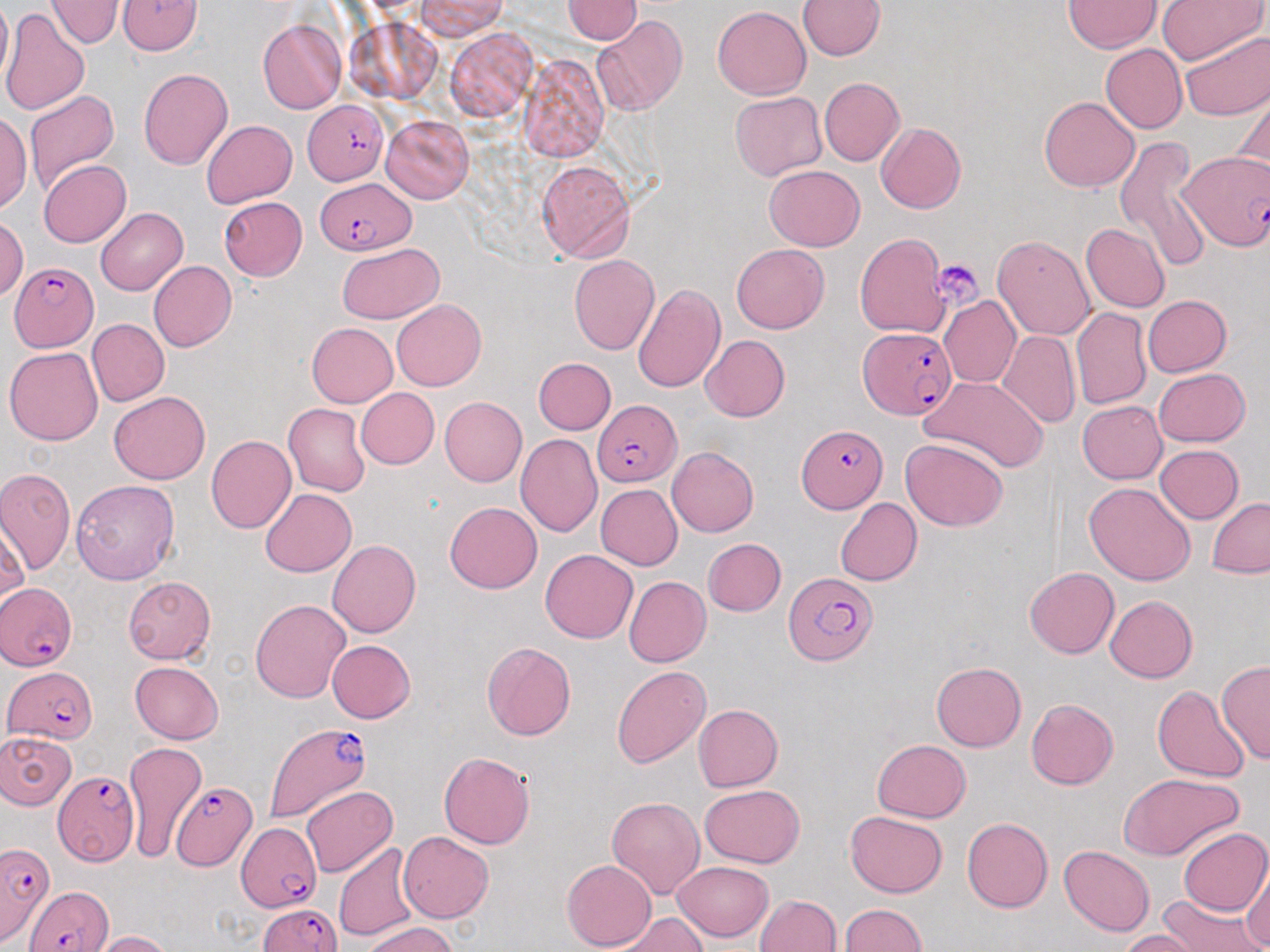
Summary:
  - Coordinate format: approximate bounding boxes as (x1, y1, x2, y2) in pixels
  - Uninfected red blood cell locations: (0, 0, 11, 91), (118, 0, 202, 55), (417, 0, 506, 39), (562, 0, 642, 45), (799, 0, 886, 60), (1155, 0, 1265, 67), (46, 1, 123, 49), (1063, 1, 1162, 53), (712, 5, 811, 98), (2, 9, 90, 115), (593, 15, 688, 118), (258, 17, 346, 114), (347, 18, 442, 104), (446, 27, 538, 122), (1180, 28, 1270, 120), (1100, 44, 1188, 133), (518, 54, 609, 161), (138, 68, 233, 170), (819, 78, 904, 166), (23, 89, 120, 198), (730, 91, 828, 182), (1234, 92, 1270, 186), (1039, 96, 1140, 192), (0, 114, 31, 211), (380, 115, 474, 203), (202, 119, 297, 208), (876, 123, 966, 213), (1114, 136, 1210, 271), (38, 160, 131, 247), (537, 161, 635, 262), (763, 166, 865, 252), (218, 196, 307, 281), (95, 207, 188, 295), (0, 216, 27, 301), (1081, 223, 1170, 313), (854, 232, 949, 339), (992, 235, 1095, 339), (337, 243, 444, 322), (731, 244, 829, 333), (569, 255, 660, 355), (149, 261, 236, 351), (632, 283, 726, 394), (939, 295, 1021, 387), (1143, 295, 1231, 378), (392, 299, 487, 391), (1071, 308, 1152, 410), (86, 319, 169, 406), (307, 323, 398, 406), (998, 330, 1080, 428), (700, 335, 791, 422), (4, 346, 103, 446), (533, 357, 616, 435), (1153, 368, 1250, 447), (918, 375, 1050, 473), (356, 388, 440, 469), (108, 393, 209, 484), (439, 397, 527, 486), (1077, 400, 1167, 483), (283, 402, 371, 497), (206, 434, 297, 533), (515, 434, 603, 536), (900, 438, 1009, 532), (1153, 444, 1245, 524), (667, 447, 759, 537), (0, 466, 75, 574), (70, 480, 179, 585), (1083, 482, 1196, 586), (595, 484, 683, 570), (261, 488, 356, 577), (835, 497, 922, 587), (1207, 498, 1270, 578), (445, 502, 542, 594), (1, 518, 30, 609), (703, 538, 785, 616), (327, 539, 421, 638), (541, 550, 638, 644), (1025, 567, 1119, 659), (122, 575, 216, 665), (623, 577, 711, 667), (1105, 595, 1197, 683), (250, 599, 351, 703), (327, 639, 414, 723), (481, 642, 576, 740), (130, 661, 223, 743), (931, 661, 1026, 751), (1216, 661, 1270, 764), (612, 666, 711, 769), (1153, 685, 1251, 783), (1026, 698, 1119, 790), (693, 704, 782, 791), (0, 731, 77, 810), (871, 740, 971, 822), (124, 742, 209, 860), (439, 752, 536, 849), (1118, 772, 1246, 862), (699, 784, 804, 867), (302, 785, 397, 877), (607, 796, 704, 900), (844, 811, 948, 897), (961, 817, 1052, 912), (1178, 826, 1270, 916), (399, 832, 494, 923), (334, 843, 421, 942), (1060, 846, 1154, 936), (561, 858, 656, 950), (672, 860, 774, 940), (1243, 863, 1270, 949), (1155, 892, 1265, 952), (755, 894, 841, 951), (838, 904, 927, 952), (615, 914, 711, 952), (363, 919, 458, 952), (1120, 930, 1200, 951), (91, 931, 173, 951)
  - Plasmodium falciparum-infected red blood cell locations: (303, 100, 388, 186), (1180, 149, 1269, 253), (316, 177, 415, 255), (8, 261, 99, 351), (858, 326, 959, 420), (592, 400, 680, 483), (797, 425, 884, 513), (782, 572, 877, 667), (1, 582, 76, 669), (5, 666, 93, 742), (262, 720, 375, 824), (49, 765, 138, 897), (171, 780, 257, 871), (235, 823, 322, 911), (0, 841, 54, 947), (25, 885, 114, 952), (258, 902, 339, 951)
  - Platelet locations: (932, 258, 983, 310)
  - Slide-level diagnosis: Plasmodium falciparum
  - Field of view: one of a larger specimen
  - Image size: 1270×952 pixels
  - Preparation: thin blood film
  - Stain: May-Grünwald-Giemsa
  - Magnification: 1000x
  - Modality: light microscopy